Name the blood parasite species.
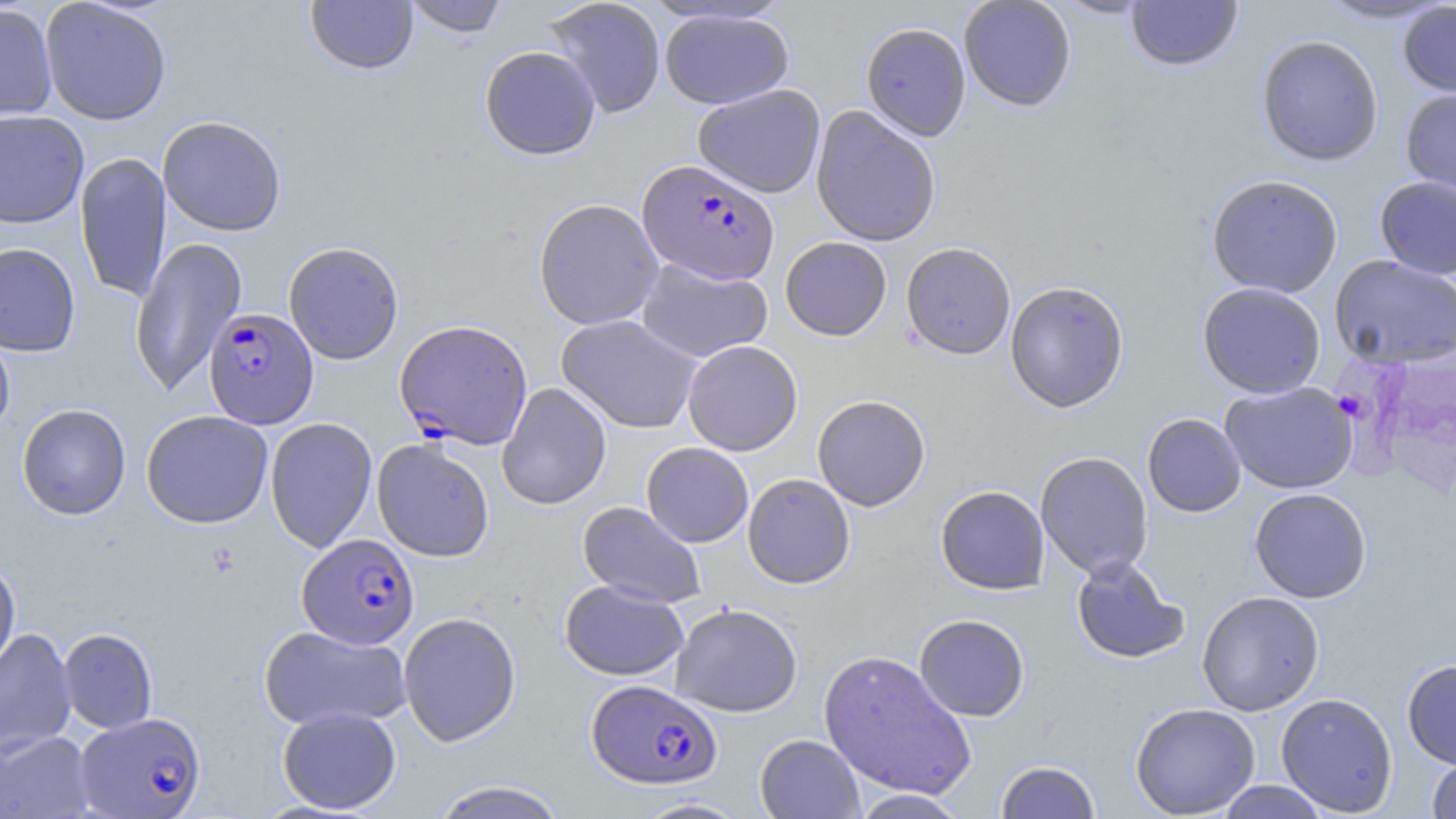

Plasmodium falciparum.

Summary:
  - Coordinate format: approximate bounding boxes as (x1,y1)-(x2,y2) corner pairs in pixels
  - Plasmodium falciparum-infected red blood cell locations: (637,159)-(779,284), (203,307)-(319,429), (394,319)-(533,450), (297,533)-(420,649), (586,679)-(722,789), (75,712)-(207,818)
  - Uninfected red blood cell locations: (40,0)-(172,125), (403,0)-(510,37), (544,0)-(666,118), (958,0)-(1076,111), (1050,0)-(1156,19), (1125,0)-(1243,71), (1314,0)-(1454,25), (305,1)-(419,75), (1398,2)-(1456,98), (0,3)-(58,122), (659,8)-(793,109), (861,22)-(971,141), (1256,34)-(1384,166), (480,46)-(601,160), (693,84)-(826,198), (1400,88)-(1456,202), (811,105)-(941,247), (0,109)-(89,229), (157,115)-(287,236), (74,151)-(171,304), (1206,174)-(1343,298), (1375,176)-(1456,280), (533,198)-(664,330), (130,236)-(248,397), (780,237)-(891,340), (283,241)-(404,365), (0,242)-(81,357), (901,242)-(1016,360), (1330,255)-(1456,368), (636,258)-(773,362), (1005,280)-(1129,412), (1197,282)-(1326,399), (556,314)-(701,433), (0,325)-(15,440), (683,340)-(802,455), (1220,381)-(1358,494), (496,382)-(612,510), (812,394)-(930,511), (17,403)-(131,520), (141,410)-(273,528), (1142,413)-(1246,517), (264,417)-(378,554), (372,438)-(495,562), (641,442)-(753,547), (1035,451)-(1154,580), (742,473)-(855,589), (935,485)-(1050,595), (1248,487)-(1372,603), (578,501)-(707,608), (1070,556)-(1190,665), (0,557)-(21,678), (560,579)-(689,681), (1197,590)-(1325,716), (670,603)-(802,717), (398,611)-(522,746), (914,614)-(1029,722), (257,624)-(411,731), (58,627)-(158,733), (0,628)-(77,757), (817,649)-(977,800), (1402,659)-(1456,769), (1275,693)-(1398,816), (1130,702)-(1261,818), (277,706)-(401,814), (0,729)-(95,818), (754,734)-(865,819), (1426,755)-(1456,818), (995,760)-(1101,818), (1214,780)-(1331,818), (427,781)-(570,818), (849,789)-(971,818), (631,797)-(752,818)
  - Preparation: thin blood film
  - Magnification: 1000x
  - Stain: May-Grünwald-Giemsa
  - Field of view: one of a larger specimen
  - Modality: light microscopy
  - Image size: 1456×819 pixels